Name the cell type shown.
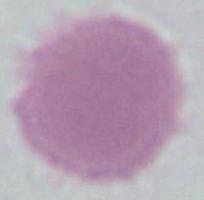

This is an erythrocyte.

modality = micrograph
magnification = 1000x